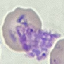

result: malaria parasites identified
stain: Giemsa
capture: smartphone through the microscope eyepiece
image_type: automatically extracted cell patch, resized to 64 × 64 pixels
preparation: thin smear